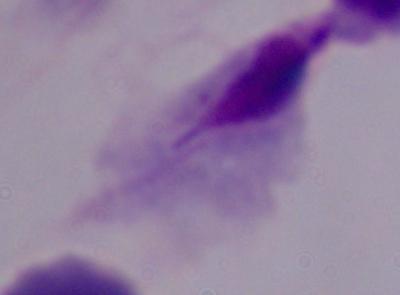 Micrograph. 1000x magnification. A trichomonad is shown.